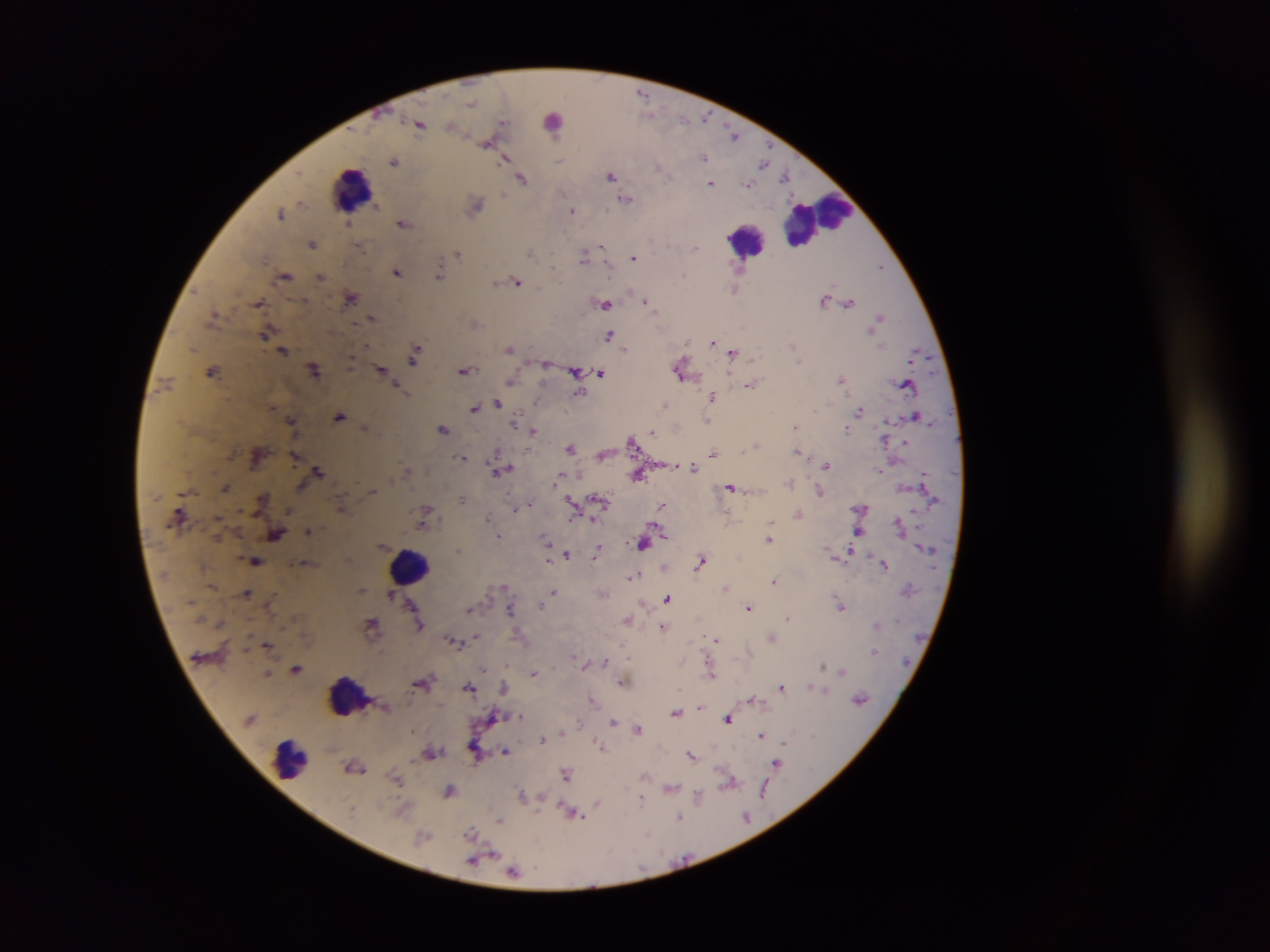

{
  "preparation": "thick blood smear",
  "image_size": "1270×952 pixels",
  "plasmodium_parasite_locations": "approximate centers as [x, y] in pixels: [643, 94], [471, 103], [705, 118], [684, 120], [503, 122], [420, 124], [452, 126], [734, 134], [487, 144], [504, 157], [704, 157], [395, 161], [763, 162], [660, 168], [611, 176], [785, 177], [522, 178], [711, 183], [748, 184], [627, 198], [476, 206], [573, 210], [281, 212], [348, 223], [404, 223], [313, 244], [602, 247], [360, 248], [697, 248], [531, 251], [458, 254], [584, 255], [634, 257], [881, 267], [741, 268], [397, 271], [439, 275], [321, 276], [285, 277], [517, 281], [496, 282], [735, 290], [351, 298], [824, 299], [305, 300], [645, 300], [259, 302], [849, 302], [605, 305], [214, 314], [879, 317], [373, 318], [266, 333], [610, 334], [713, 341], [366, 345], [793, 346], [510, 349], [626, 349], [283, 350], [733, 353], [415, 356], [351, 364], [213, 370], [315, 370], [381, 370], [466, 370], [576, 370], [680, 371], [601, 373], [841, 378], [511, 381], [751, 385], [905, 385], [399, 388], [577, 394], [713, 396], [498, 403], [665, 405], [474, 408], [815, 410], [860, 411], [340, 415], [916, 416], [291, 419], [708, 420], [515, 421], [365, 427], [795, 427], [847, 428], [443, 430], [533, 431], [652, 432], [885, 440], [632, 441], [905, 443], [757, 445], [571, 447], [798, 451], [713, 454], [296, 456], [462, 457], [826, 465], [694, 467], [319, 471], [501, 471], [638, 475], [557, 479], [790, 481], [731, 487], [225, 488], [373, 491], [819, 491], [462, 499], [262, 500], [599, 500], [573, 502], [528, 504], [663, 505], [341, 507], [515, 509], [798, 513], [425, 516], [488, 518], [898, 522], [771, 523], [309, 530], [276, 534], [498, 536], [768, 539], [546, 540], [644, 543], [459, 550], [598, 551], [848, 552], [567, 554], [255, 561], [701, 561], [884, 564], [634, 575], [775, 580], [725, 588], [362, 590], [554, 591], [247, 593], [392, 594], [603, 594], [668, 599], [540, 605], [841, 606], [748, 607], [470, 609], [510, 609], [788, 617], [627, 620], [373, 624], [420, 625], [663, 626], [477, 637], [772, 637], [716, 639], [453, 641], [268, 645], [874, 651], [574, 656], [606, 663], [583, 664], [823, 665], [296, 668], [483, 668], [843, 671], [534, 673], [711, 674], [422, 682], [621, 682], [469, 687], [505, 687], [781, 687], [811, 687], [824, 691], [592, 699], [752, 699], [860, 700], [700, 707], [676, 713], [522, 717], [729, 720], [614, 722], [579, 723], [638, 729], [563, 732], [762, 735], [541, 740], [783, 742], [601, 746], [505, 751], [431, 753], [692, 755], [776, 764], [354, 767], [567, 774], [645, 776], [396, 781], [730, 782], [671, 788], [450, 791], [763, 792], [522, 793], [699, 796], [642, 799], [598, 804], [575, 815], [680, 817], [746, 817], [499, 820], [472, 833], [423, 836], [474, 860], [514, 871]",
  "field_of_view": "single",
  "capture": "mobile-phone photograph through a microscope",
  "country": "Ghana",
  "leukocyte_locations": "approximate centers as [x, y] in pixels: [561, 119], [352, 189], [819, 219], [749, 239], [409, 565], [347, 696], [287, 758]"
}